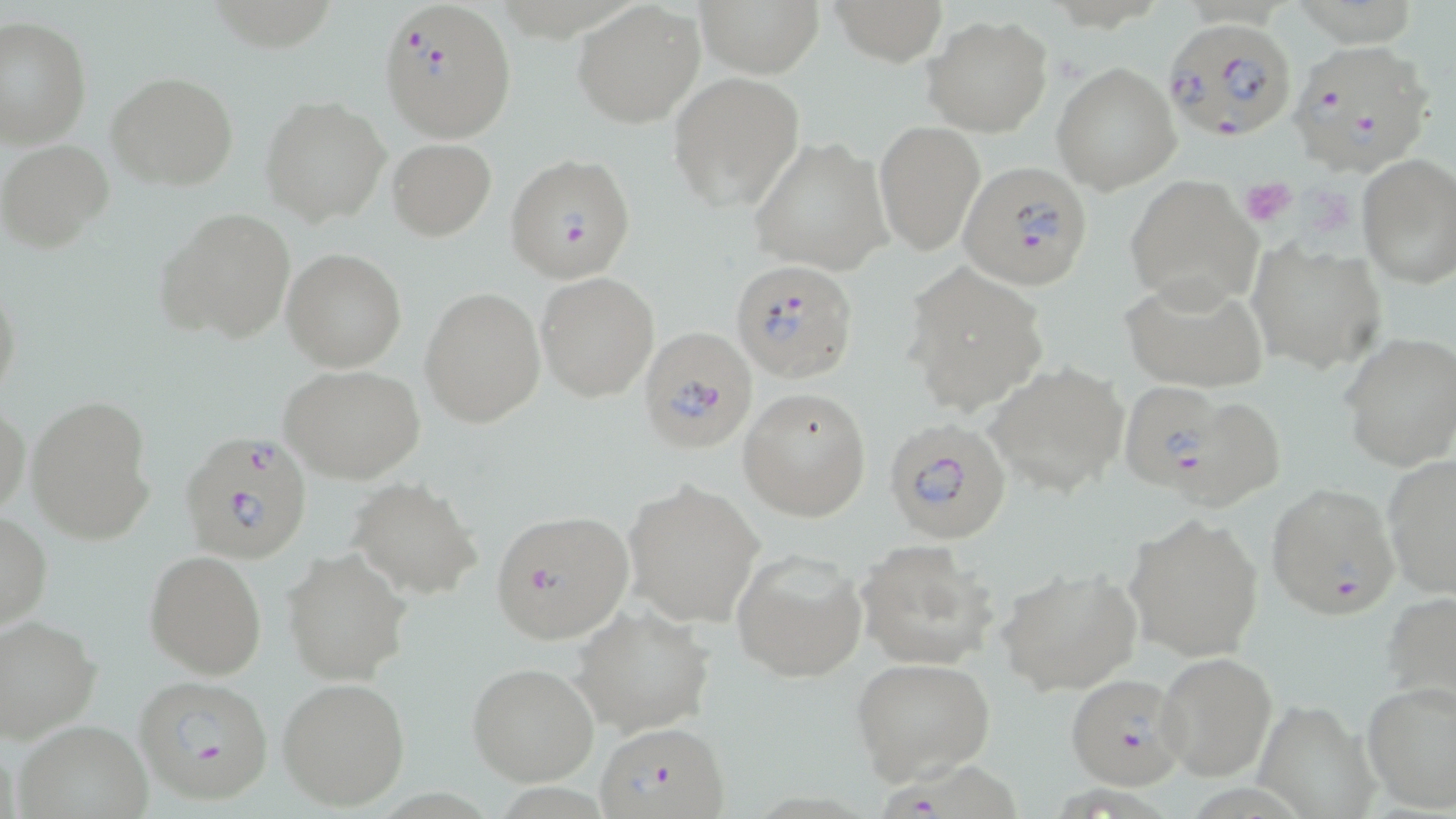 Approximate bounding boxes as [x1, y1, x2, y2] in pixels. Platelet locations: [1241, 179, 1297, 227], [1310, 189, 1353, 240]. Plasmodium falciparum-infected red blood cell locations: [379, 0, 516, 141], [1161, 18, 1296, 140], [1287, 37, 1436, 178], [510, 156, 641, 284], [959, 160, 1093, 290], [732, 259, 859, 384], [638, 326, 758, 454], [1116, 380, 1239, 498], [881, 418, 1012, 542], [177, 432, 316, 565], [1266, 482, 1400, 619], [489, 508, 635, 644], [1066, 672, 1188, 789], [134, 674, 276, 804], [595, 718, 732, 819], [877, 751, 1026, 818]. Uninfected red blood cell locations: [694, 0, 822, 77], [827, 0, 949, 66], [572, 3, 703, 127], [925, 16, 1052, 135], [0, 17, 91, 148], [1051, 63, 1181, 192], [106, 70, 239, 190], [668, 71, 805, 213], [261, 97, 390, 227], [874, 119, 984, 255], [748, 137, 889, 275], [1, 139, 113, 251], [388, 139, 496, 240], [1356, 154, 1456, 288], [1123, 175, 1262, 309], [156, 208, 295, 343], [1247, 243, 1388, 374], [282, 249, 406, 372], [905, 261, 1049, 416], [537, 273, 658, 401], [1120, 274, 1269, 394], [0, 279, 24, 411], [420, 289, 545, 429], [1340, 333, 1456, 472], [986, 362, 1130, 495], [280, 364, 425, 482], [738, 388, 872, 522], [1151, 388, 1289, 513], [25, 393, 156, 545], [1, 400, 29, 518], [1381, 455, 1456, 597], [349, 478, 484, 600], [623, 480, 763, 625], [1, 511, 51, 633], [1122, 511, 1265, 661], [856, 539, 999, 670], [732, 548, 869, 683], [283, 549, 412, 686], [145, 550, 267, 679], [996, 567, 1143, 694], [1380, 590, 1456, 715], [574, 605, 715, 737], [0, 614, 101, 743], [1156, 651, 1277, 782], [852, 657, 994, 783], [466, 661, 599, 785], [279, 677, 411, 811], [1362, 679, 1456, 813], [1251, 697, 1384, 819], [17, 722, 151, 815]. Slide-level diagnosis: Plasmodium falciparum. May-Grünwald-Giemsa stain. 1000x magnification. Thin blood smear. Image is 1456×819 pixels. Optical microscopy. Single field of view.